Identify the parasite.
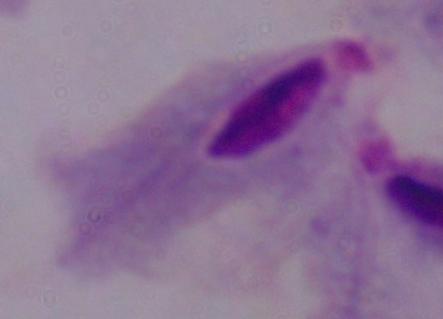
A trichomonad.

Micrograph. 1000x magnification.